Locate and identify every blood parasite.
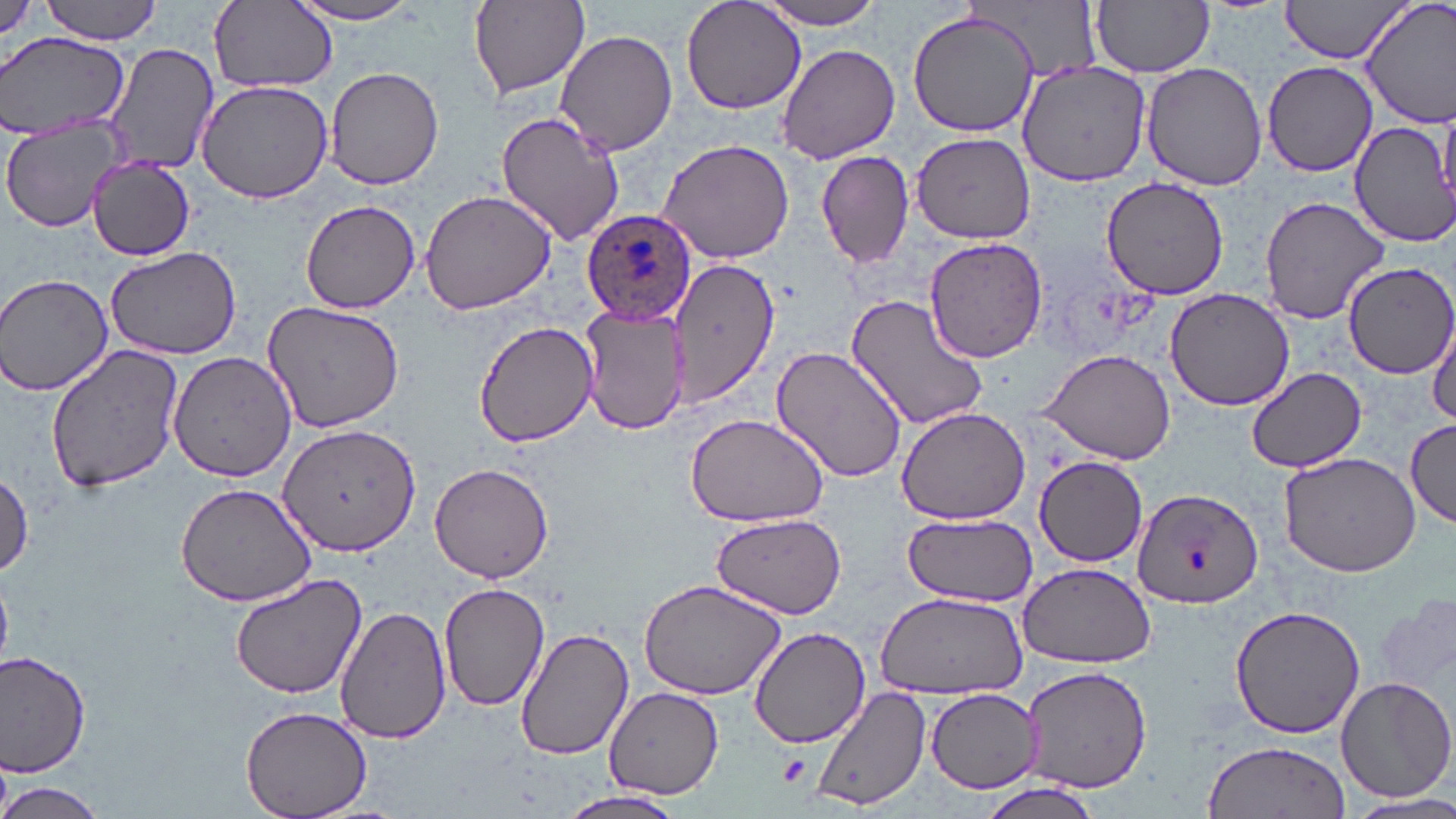
Approximate bounding boxes as (x1, y1, x2, y2) in pixels.
Plasmodium ovale-infected red blood cells: (582, 214, 696, 330).
No Plasmodium falciparum, Plasmodium malariae, Plasmodium vivax, Babesia divergens, or Trypanosoma brucei observed.

Platelet locations: (778, 751, 810, 784). Uninfected red blood cell locations: (41, 0, 163, 44), (468, 0, 590, 99), (680, 0, 807, 116), (753, 0, 889, 29), (1092, 0, 1214, 78), (1277, 0, 1415, 64), (1361, 0, 1456, 125), (209, 1, 337, 95), (283, 1, 432, 27), (907, 9, 1038, 136), (553, 28, 677, 155), (0, 33, 129, 139), (101, 41, 220, 174), (776, 43, 900, 164), (1017, 61, 1149, 186), (1261, 61, 1377, 176), (1141, 62, 1270, 190), (325, 67, 445, 188), (195, 79, 336, 204), (495, 110, 625, 248), (1346, 113, 1454, 246), (1, 119, 127, 233), (910, 133, 1034, 243), (658, 138, 794, 263), (815, 149, 915, 270), (88, 156, 194, 261), (1100, 176, 1229, 300), (419, 188, 556, 316), (1257, 193, 1390, 326), (299, 199, 420, 314), (923, 238, 1048, 363), (104, 246, 241, 360), (666, 256, 779, 408), (1345, 262, 1456, 379), (0, 274, 114, 395), (1165, 287, 1294, 410), (845, 289, 991, 434), (261, 299, 405, 433), (580, 305, 689, 436), (473, 321, 598, 446), (1428, 323, 1456, 429), (44, 344, 186, 493), (770, 344, 910, 485), (1038, 349, 1177, 464), (167, 353, 298, 481), (1246, 366, 1368, 474), (896, 407, 1030, 525), (683, 410, 831, 528), (1405, 416, 1456, 526), (278, 425, 419, 555), (1277, 448, 1425, 576), (1035, 456, 1148, 566), (430, 462, 554, 583), (0, 471, 33, 581), (177, 481, 315, 605), (1130, 486, 1262, 611), (708, 513, 847, 617), (899, 517, 1043, 605), (1018, 562, 1155, 669), (229, 570, 369, 699), (636, 577, 788, 700), (439, 579, 550, 713), (872, 592, 1029, 699), (1377, 594, 1453, 702), (1229, 605, 1366, 739), (335, 607, 451, 743), (515, 627, 633, 760), (749, 627, 873, 749), (0, 649, 93, 777), (1021, 665, 1152, 792), (1335, 675, 1455, 803), (811, 685, 929, 812), (603, 686, 724, 799), (923, 688, 1044, 794), (240, 705, 374, 818), (1200, 740, 1351, 819), (971, 779, 1107, 819), (0, 781, 109, 819), (553, 790, 688, 819), (1346, 792, 1456, 818). Slide-level diagnosis: Plasmodium ovale. Image is 1456×819 pixels. Optical microscopy. May-Grünwald-Giemsa stain. Thin blood smear. Single field of view. Captured at 1000x magnification.